Locate every malaria parasite and every leukocyte.
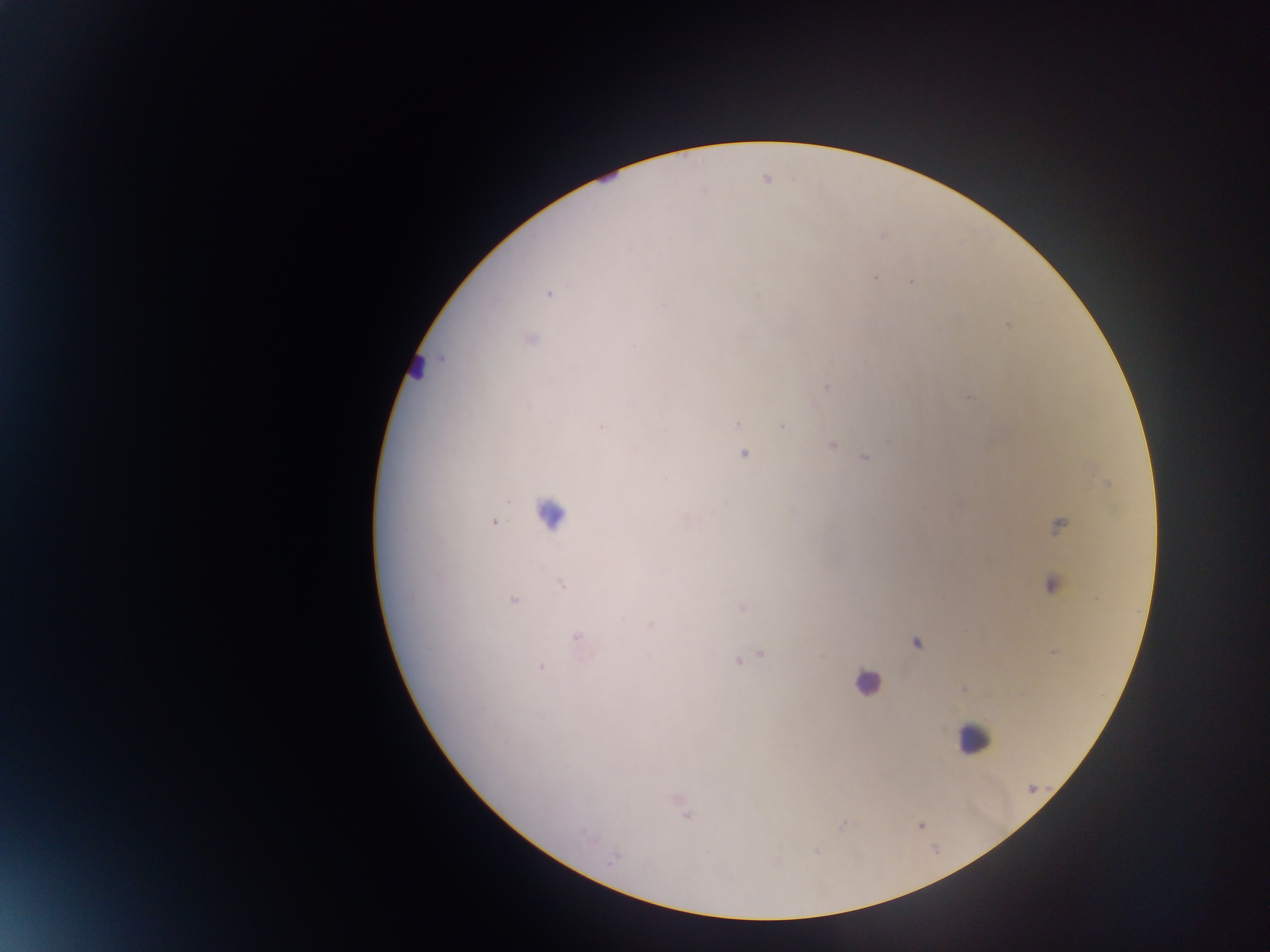
Approximate centers as x y in pixels.
Malaria parasites: 702 191; 875 276; 911 281; 1007 326; 633 344; 826 386; 967 398; 738 423; 783 424; 601 425; 831 445; 744 453; 863 456; 494 522; 560 583; 513 600; 576 637; 761 654; 738 660; 540 668; 612 857.
Leukocytes: 549 514; 870 690; 971 737.

Summary:
  - Image size: 1270×952 pixels
  - Field of view: single
  - Capture: mobile-phone photograph through a microscope
  - Preparation: thick blood smear
  - Country: Ghana